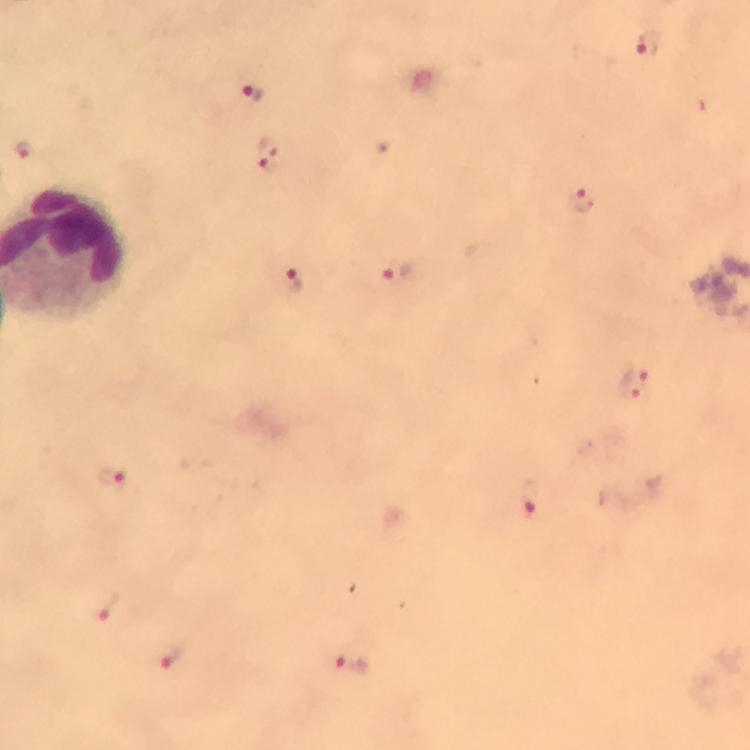
{
  "image_size": "750×750 pixels",
  "immersion_oil": "applied",
  "context": "from a diagnostic examination for malaria",
  "stain": "Giemsa",
  "malaria_parasite_locations": "approximate centers as (x, y) in pixels: (647, 45), (252, 92), (22, 148), (267, 151), (584, 199), (396, 273), (291, 285), (633, 383), (112, 476), (531, 499), (107, 607), (172, 654), (351, 663)",
  "cropped_from": "a single field of view",
  "magnification": "100x",
  "capture": "smartphone camera through the microscope",
  "preparation": "thick blood film"
}